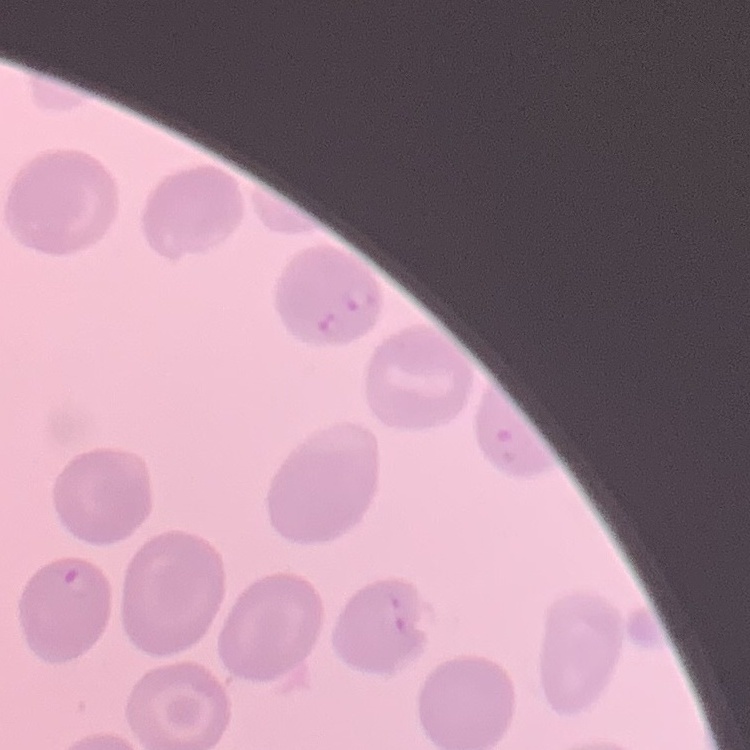
Summary:
  - Erythrocyte morphology: no rouleaux formation
  - Image type: one tile cut from a larger photomicrograph
  - Stain: Field's or Giemsa
  - Preparation: thin blood film